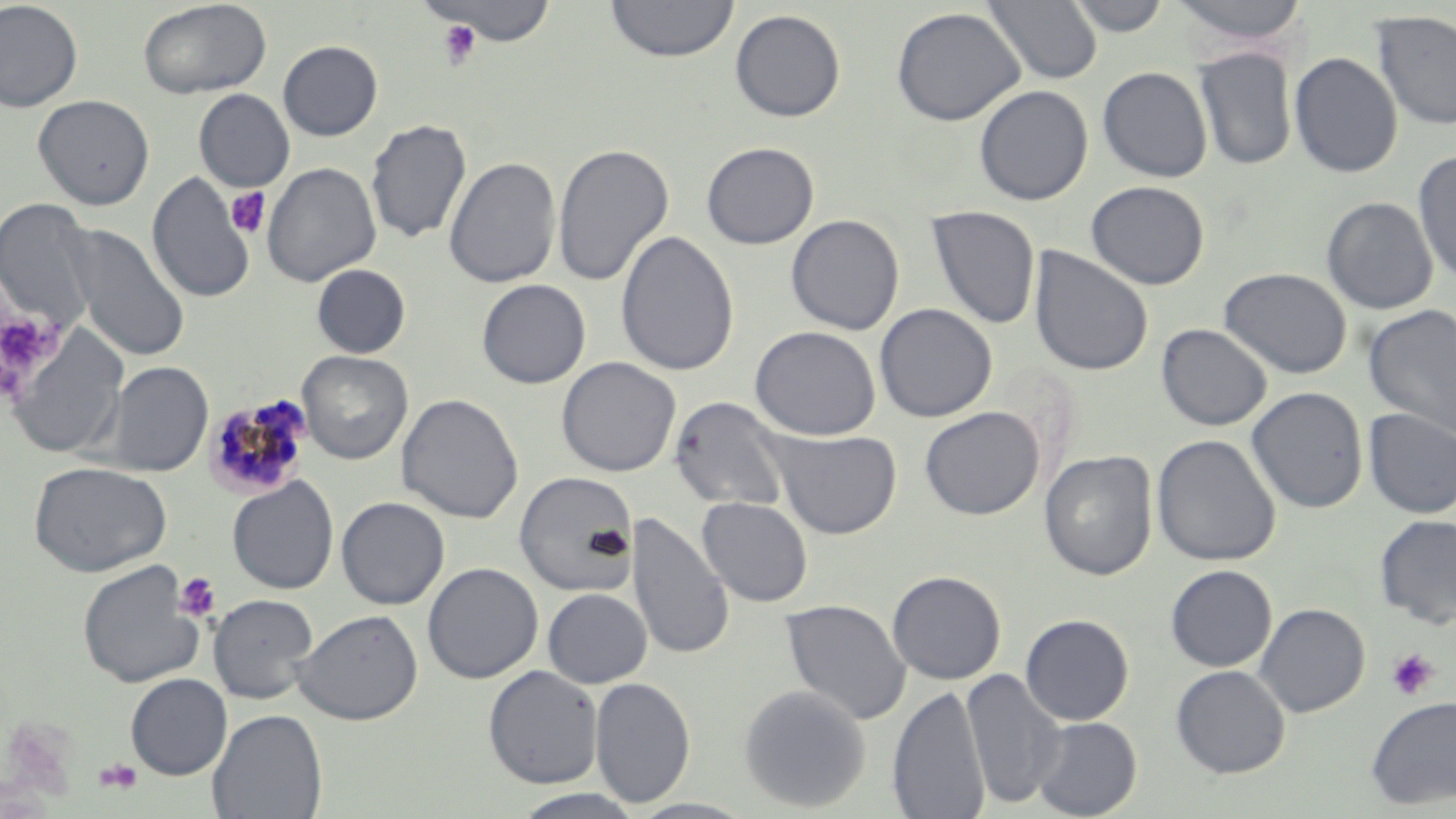
slide_level_diagnosis: Plasmodium malariae
image_size: 1456×819 pixels
preparation: thin blood film
uninfected_red_blood_cell_locations: 'approximate bounding boxes as (x1,y1)-(x2,y2) corner pairs in pixels: (138,0)-(272,99), (425,0)-(558,46), (605,0)-(739,62), (983,0)-(1102,85), (1065,0)-(1172,37), (1169,0)-(1310,51), (0,1)-(83,112), (891,7)-(1025,126), (729,9)-(846,122), (1371,10)-(1456,130), (278,40)-(383,141), (1194,47)-(1297,171), (1288,51)-(1403,178), (1097,66)-(1212,182), (973,84)-(1093,205), (193,89)-(295,192), (33,94)-(155,210), (366,119)-(471,245), (701,141)-(819,249), (553,142)-(674,287), (1413,150)-(1456,286), (443,157)-(561,289), (262,162)-(382,287), (147,172)-(256,304), (1085,180)-(1210,289), (1321,196)-(1438,314), (0,198)-(99,332), (925,205)-(1040,329), (785,214)-(904,335), (67,225)-(190,362), (616,229)-(739,378), (1029,247)-(1153,376), (311,264)-(411,358), (1219,267)-(1352,379), (477,279)-(591,389), (874,303)-(997,422), (1362,304)-(1456,440), (1156,323)-(1272,431), (750,326)-(881,440), (5,329)-(130,460), (298,351)-(413,464), (556,356)-(681,477), (102,362)-(213,477), (1246,387)-(1368,513), (397,392)-(523,524), (669,396)-(791,514), (920,407)-(1044,519), (1362,408)-(1456,519), (764,427)-(902,539), (1151,434)-(1281,566), (1039,450)-(1158,581), (28,461)-(172,577), (514,471)-(638,596), (227,476)-(339,594), (336,496)-(450,609), (697,496)-(813,607), (629,512)-(733,662), (1375,514)-(1456,629), (77,560)-(205,689), (423,562)-(543,684), (1165,564)-(1277,671), (887,570)-(1006,684), (542,588)-(652,688), (208,593)-(319,704), (781,598)-(911,726), (1254,602)-(1370,717), (292,608)-(423,726), (1020,613)-(1134,725), (483,665)-(603,788), (1171,665)-(1290,778), (962,668)-(1066,809), (125,673)-(232,779), (590,676)-(695,807), (738,683)-(871,812), (887,684)-(990,819), (1365,694)-(1456,809), (207,708)-(328,819), (1030,716)-(1142,818), (510,789)-(646,818)'
field_of_view: one of a larger specimen
modality: optical microscopy
stain: May-Grünwald-Giemsa
platelet_locations: 'approximate bounding boxes as (x1,y1)-(x2,y2) corner pairs in pixels: (436,18)-(481,70), (225,187)-(271,239), (0,306)-(64,386), (173,571)-(221,623), (1385,648)-(1439,700), (92,758)-(143,794)'
plasmodium_malariae_infected_red_blood_cell_locations: 'approximate bounding boxes as (x1,y1)-(x2,y2) corner pairs in pixels: (202,393)-(313,499)'
magnification: 1000x